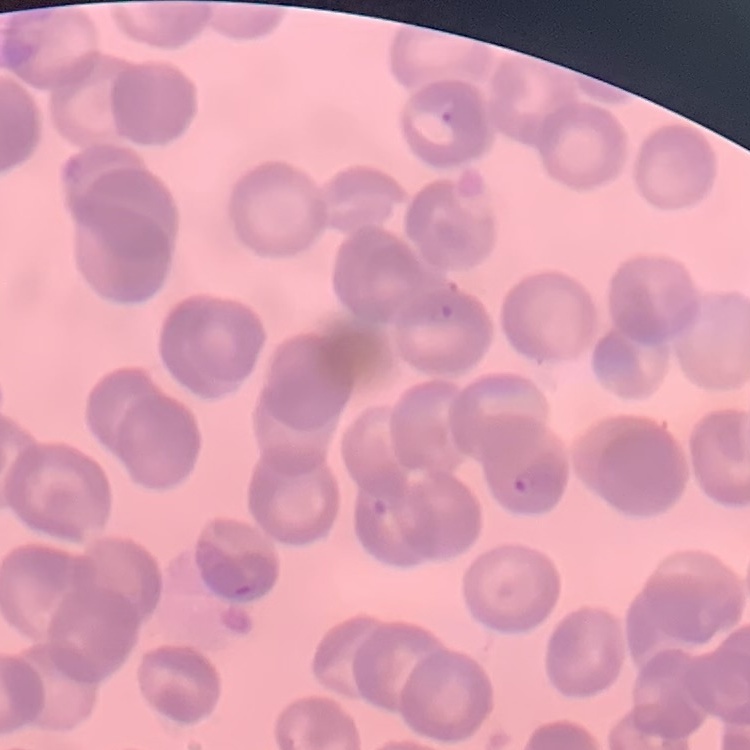

The erythrocytes exhibit rouleaux formation. Thin peripheral smear. Field's or Giemsa stain. Square crop of a larger photomicrograph.